Name the parasite shown.
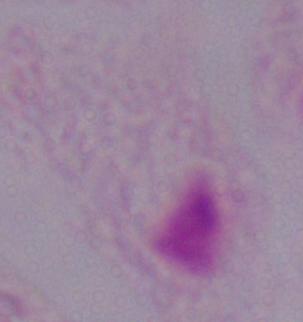

This is a trichomonad.

magnification = 1000x
modality = photomicrograph